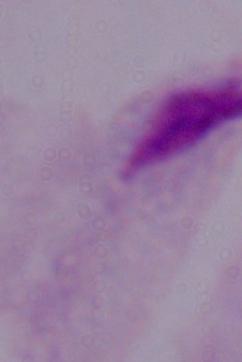

A trichomonad is shown. Captured at 1000x magnification. Micrograph.